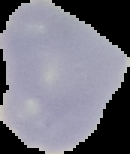

Summary:
  - Image size: 130×154 pixels
  - Malaria status: uninfected
  - Image type: segmented cell region on a black background
  - Preparation: thin blood film